Name the parasite shown.
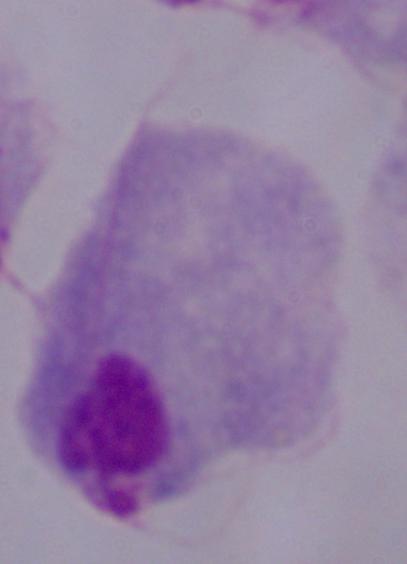
A trichomonad.

modality: micrograph
magnification: 1000x